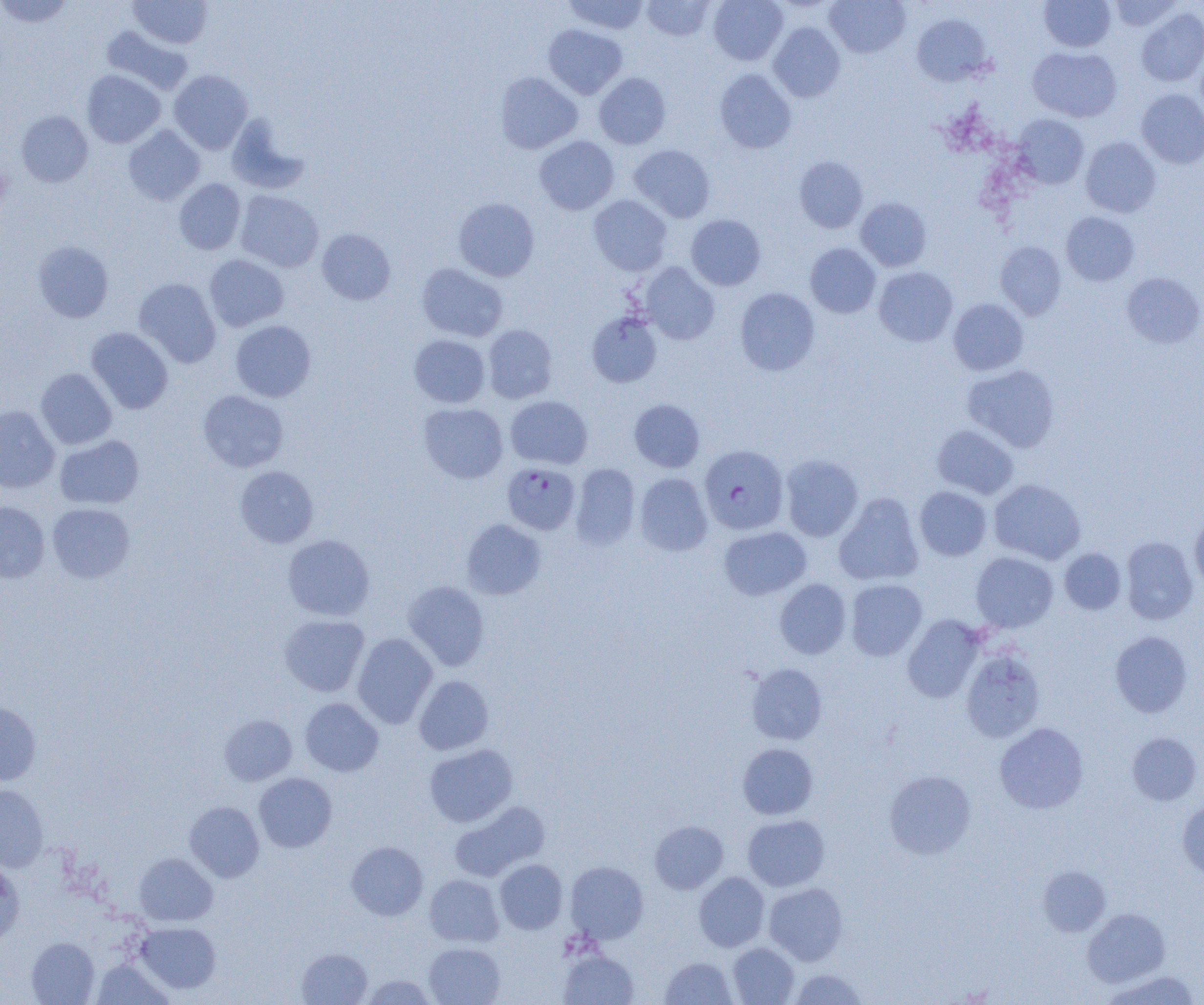

slide_level_diagnosis: Plasmodium falciparum
magnification: 1000x
image_size: 1204×1005 pixels
preparation: thin blood film
field_of_view: single
uninfected_red_blood_cell_locations: 'approximate bounding boxes as (x1, y1, x2, y2) in pixels: (0, 0, 74, 28), (564, 0, 649, 34), (641, 0, 715, 41), (708, 0, 788, 65), (825, 0, 910, 58), (1108, 0, 1181, 31), (129, 1, 213, 48), (1040, 1, 1115, 52), (1136, 8, 1204, 86), (912, 14, 993, 85), (768, 22, 845, 102), (543, 24, 628, 98), (102, 25, 193, 95), (1027, 47, 1122, 122), (714, 69, 796, 154), (82, 70, 165, 148), (170, 70, 252, 155), (495, 72, 582, 154), (594, 73, 670, 149), (1136, 89, 1204, 168), (16, 111, 93, 187), (227, 114, 309, 194), (1012, 114, 1089, 188), (123, 125, 205, 205), (534, 135, 619, 215), (1080, 136, 1162, 217), (629, 144, 715, 222), (794, 156, 867, 233), (174, 179, 246, 255), (235, 190, 324, 272), (589, 195, 672, 276), (453, 197, 540, 282), (856, 197, 932, 271), (1061, 212, 1139, 286), (686, 215, 766, 291), (317, 228, 396, 305), (33, 240, 114, 322), (995, 242, 1066, 320), (805, 243, 881, 318), (204, 254, 289, 331), (638, 262, 719, 345), (417, 263, 508, 342), (874, 266, 958, 346), (1121, 272, 1204, 348), (134, 277, 221, 368), (735, 287, 820, 375), (948, 298, 1028, 375), (587, 312, 662, 387), (230, 320, 316, 402), (482, 324, 558, 404), (86, 327, 173, 414), (409, 334, 490, 408), (963, 364, 1060, 452), (36, 368, 116, 449), (198, 390, 289, 472), (505, 395, 593, 469), (629, 398, 705, 472), (418, 403, 508, 483), (0, 405, 60, 494), (932, 424, 1018, 499), (55, 435, 144, 509), (781, 454, 863, 541), (571, 464, 640, 550), (235, 466, 319, 548), (635, 473, 713, 556), (989, 479, 1086, 565), (914, 486, 992, 561), (834, 493, 924, 586), (0, 500, 50, 582), (47, 502, 135, 583), (1189, 514, 1204, 595), (461, 518, 546, 600), (719, 526, 811, 600), (282, 534, 375, 621), (1120, 536, 1198, 624), (1060, 548, 1126, 614), (970, 552, 1058, 633), (774, 579, 851, 659), (845, 579, 927, 660), (403, 580, 489, 671), (279, 614, 369, 697), (903, 615, 985, 703), (1110, 631, 1192, 717), (352, 633, 438, 728), (960, 648, 1045, 743), (746, 663, 828, 745), (414, 675, 494, 755), (300, 698, 384, 776), (0, 702, 41, 785), (220, 715, 296, 785), (994, 722, 1089, 814), (1127, 732, 1202, 805), (737, 743, 818, 819), (424, 744, 518, 827), (884, 770, 976, 859), (254, 773, 336, 852), (0, 784, 48, 872), (449, 800, 550, 881), (1177, 800, 1204, 880), (184, 801, 264, 882), (743, 814, 829, 891), (650, 820, 728, 894), (346, 841, 428, 920), (134, 852, 218, 925), (494, 859, 567, 934), (565, 861, 649, 943), (0, 862, 25, 947), (1038, 866, 1111, 936), (694, 872, 769, 951), (425, 874, 504, 947), (764, 883, 847, 965), (1082, 908, 1170, 987), (137, 922, 221, 994), (26, 937, 99, 1005), (423, 942, 505, 1005), (728, 942, 799, 1004), (297, 948, 372, 1004), (559, 950, 639, 1005), (660, 957, 737, 1004), (92, 960, 173, 1004), (789, 969, 868, 1004), (1103, 971, 1200, 1005), (362, 974, 435, 1004)'
modality: optical microscopy
plasmodium_falciparum_infected_red_blood_cell_locations: 'approximate bounding boxes as (x1, y1, x2, y2) in pixels: (700, 445, 789, 534), (502, 462, 580, 534)'